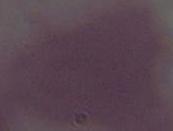
A red blood cell is shown. Micrograph. 1000x magnification.